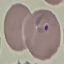 Result: malaria parasites identified. Thin blood smear. Photographed with a smartphone camera at the microscope eyepiece. Cell patch, automatically extracted from a larger field of view and resized to 64 × 64 pixels. Giemsa-stained preparation.